Point out each leukocyte.
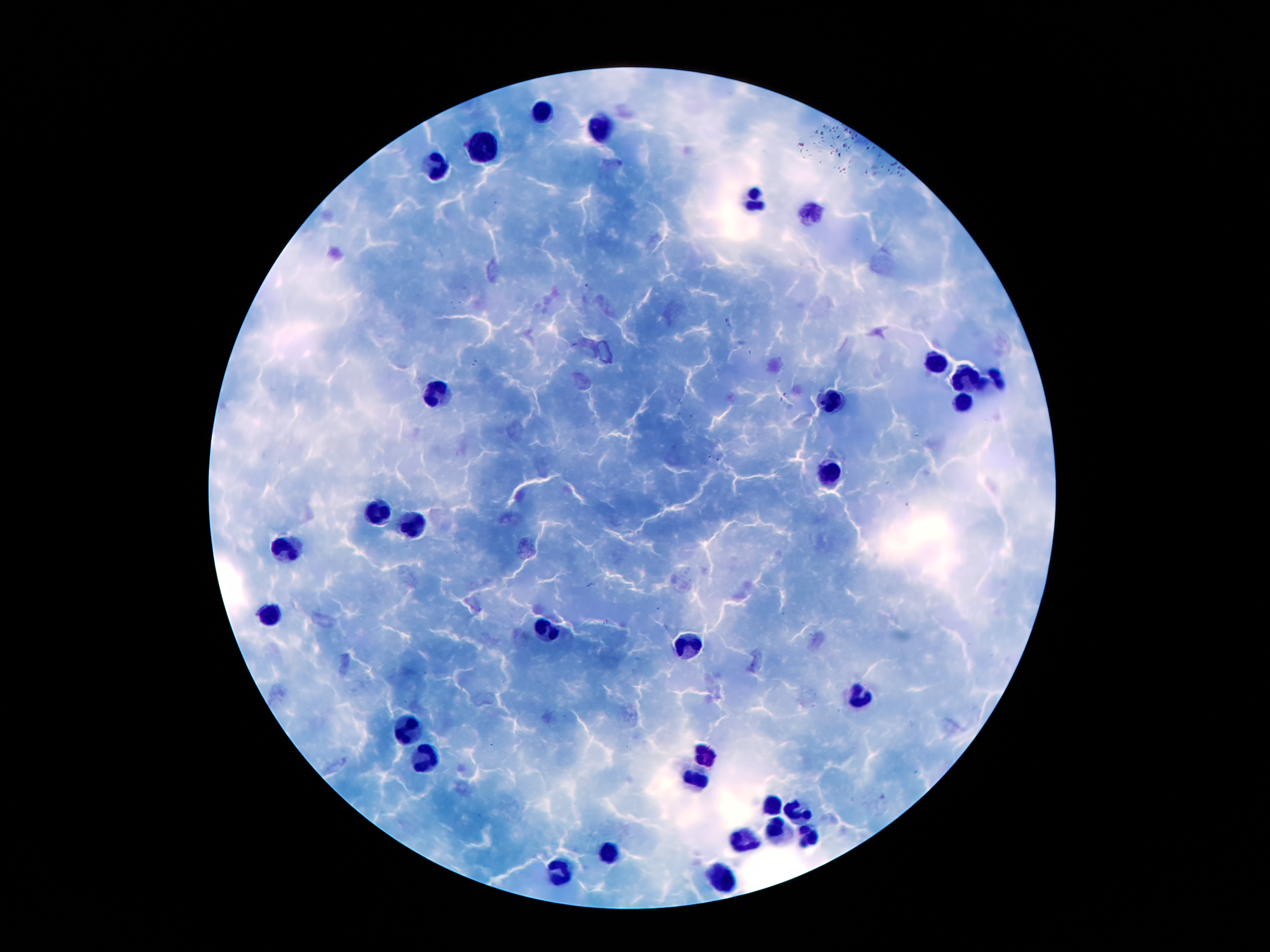
Approximate object centers, in pixels from the top-left corner.
Leukocytes: (x=545, y=111), (x=607, y=129), (x=485, y=151), (x=438, y=169), (x=754, y=197), (x=810, y=212), (x=933, y=367), (x=963, y=381), (x=993, y=383), (x=436, y=396), (x=830, y=400), (x=960, y=403), (x=833, y=475), (x=380, y=514), (x=413, y=526), (x=286, y=549), (x=270, y=615), (x=545, y=633), (x=685, y=644), (x=858, y=695), (x=410, y=732), (x=421, y=751), (x=706, y=753), (x=695, y=774), (x=772, y=804), (x=798, y=812), (x=775, y=832), (x=807, y=835), (x=741, y=840), (x=609, y=857), (x=566, y=873), (x=723, y=878).

Summary:
  - Malaria parasite locations: (x=587, y=286), (x=726, y=320), (x=474, y=363), (x=709, y=457), (x=718, y=460)
  - Patient malaria status: positive for Plasmodium falciparum
  - Field of view: one from this slide
  - Stain: Giemsa
  - Image size: 1270×952 pixels
  - Capture: smartphone camera through the microscope eyepiece
  - Preparation: thick blood smear
  - Magnification: 100x